Describe the morphology of the red blood cells.
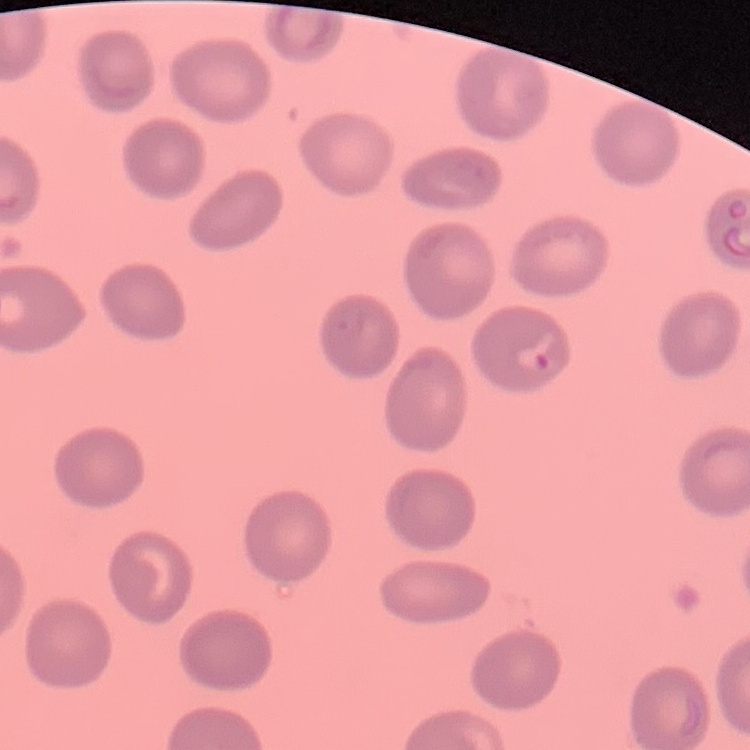
They show no rouleaux formation.

Summary:
  - Stain: Field's or Giemsa
  - Image type: one tile cut from a larger photomicrograph
  - Preparation: thin blood film